Assess for Plasmodium parasites.
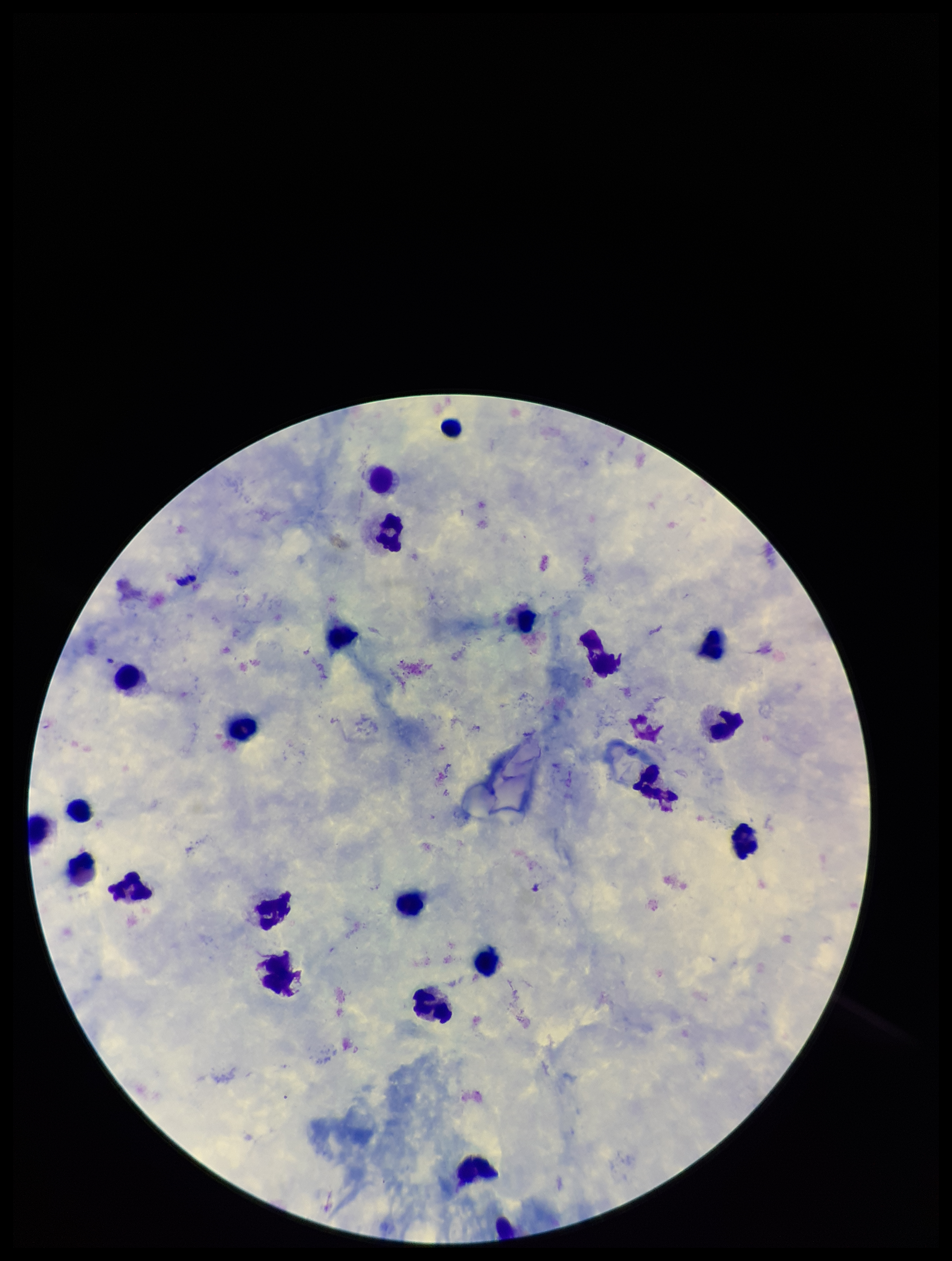
None identified.

Summary:
  - Parasite count: 0
  - Stain: Giemsa
  - Species reported for this patient: Plasmodium falciparum
  - Image size: 952×1261 pixels
  - Leukocyte count: 22
  - Preparation: thick smear
  - Capture: smartphone photograph through the microscope eyepiece
  - Patient malaria status: infected
  - Field of view: single